Describe the morphology of the red blood cells.
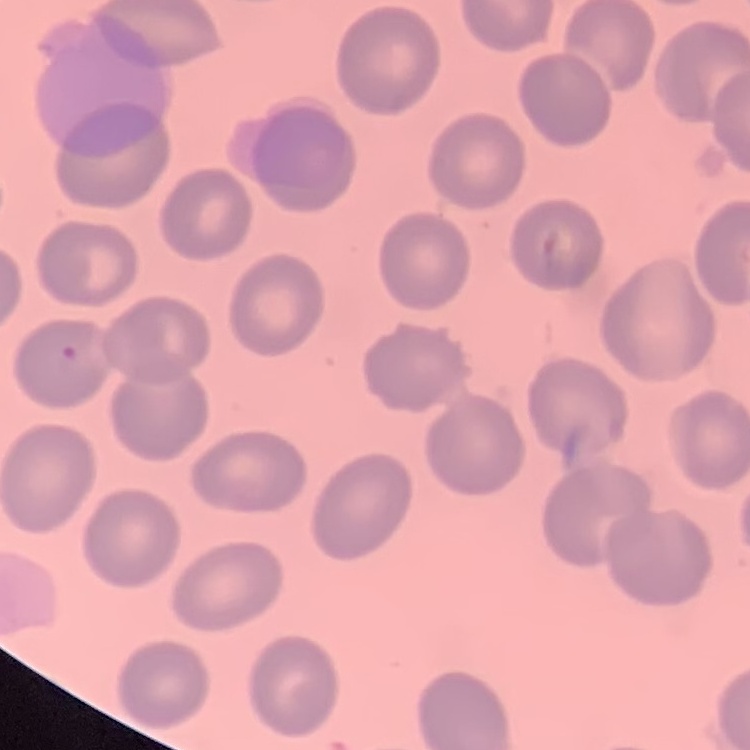

They show no rouleaux formation.

Summary:
  - Image type: square crop of a larger photomicrograph
  - Stain: Field's or Giemsa
  - Preparation: thin peripheral smear